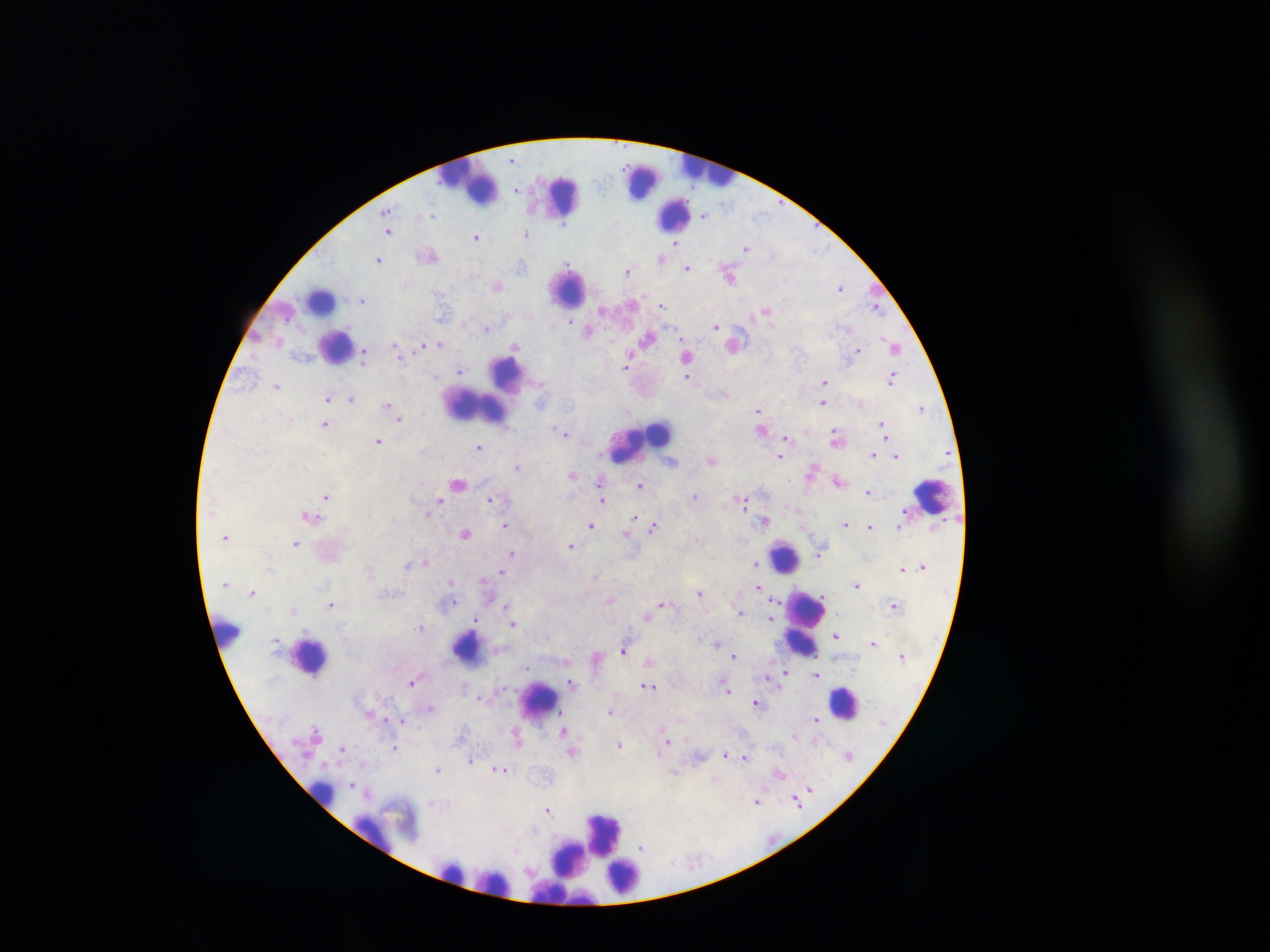
capture: mobile-phone photograph through a microscope
image_size: 1270×952 pixels
field_of_view: single
leukocyte_locations: 'approximate centers as (x, y) in pixels: (710, 174), (642, 178), (467, 189), (562, 195), (674, 216), (570, 289), (321, 303), (333, 345), (514, 366), (485, 406), (640, 442), (931, 498), (784, 558), (809, 624), (228, 634), (463, 644), (311, 652), (536, 700), (849, 702), (321, 795), (606, 834), (447, 865), (631, 874), (492, 883), (557, 891)'
country: Ghana
malaria_parasite_locations: 'approximate centers as (x, y) in pixels: (513, 159), (517, 187), (519, 190), (430, 216), (704, 216), (426, 218), (565, 227), (388, 231), (527, 234), (477, 237), (677, 243), (747, 248), (819, 250), (774, 256), (662, 258), (377, 259), (569, 265), (687, 266), (521, 268), (629, 272), (728, 274), (497, 287), (841, 287), (362, 300), (629, 304), (877, 305), (661, 306), (442, 307), (767, 309), (604, 311), (575, 319), (570, 321), (716, 326), (486, 328), (589, 330), (846, 330), (647, 337), (889, 342), (393, 344), (440, 344), (422, 345), (734, 345), (514, 347), (895, 349), (858, 350), (630, 351), (365, 353), (688, 356), (626, 358), (459, 368), (625, 368), (892, 376), (687, 378), (823, 382), (275, 386), (352, 398), (327, 399), (823, 403), (388, 406), (758, 409), (923, 409), (399, 414), (401, 418), (884, 423), (325, 426), (553, 427), (884, 429), (833, 432), (566, 434), (885, 435), (787, 438), (377, 440), (479, 448), (874, 455), (897, 456), (780, 457), (712, 461), (517, 467), (811, 473), (572, 474), (600, 481), (459, 484), (640, 484), (867, 492), (442, 494), (695, 496), (326, 497), (741, 497), (489, 499), (439, 500), (603, 501), (743, 501), (797, 509), (634, 518), (767, 522), (846, 524), (505, 526), (591, 526), (869, 527), (654, 528), (465, 532), (627, 536), (294, 543), (571, 545), (511, 552), (822, 553), (424, 563), (756, 564), (406, 565), (271, 566), (502, 574), (596, 575), (449, 581), (758, 586), (252, 592), (701, 592), (610, 601), (776, 601), (504, 602), (452, 603), (663, 605), (330, 606), (292, 611), (740, 614), (647, 616), (773, 619), (475, 622), (513, 625), (422, 627), (836, 635), (717, 643), (623, 652), (731, 652), (735, 654), (648, 661), (525, 670), (785, 670), (313, 675), (817, 676), (766, 677), (571, 682), (411, 683), (650, 686), (463, 687), (728, 692), (481, 697), (756, 702), (430, 709), (609, 710), (813, 719), (401, 721), (564, 732), (316, 736), (669, 741), (816, 742), (517, 745), (621, 746), (342, 750), (393, 750), (573, 754), (724, 755), (847, 756), (744, 757), (470, 761), (438, 770), (501, 770), (676, 773), (780, 776), (717, 781), (352, 782), (810, 787), (807, 791), (796, 800), (755, 801), (433, 804), (798, 805), (548, 811), (536, 830), (641, 846), (517, 851)'
preparation: thick blood smear